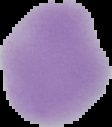

From a thin blood film. Image is 112×127 pixels. The area outside the segmented cell region is set to black. Malaria status: uninfected.